Name the blood parasite species.
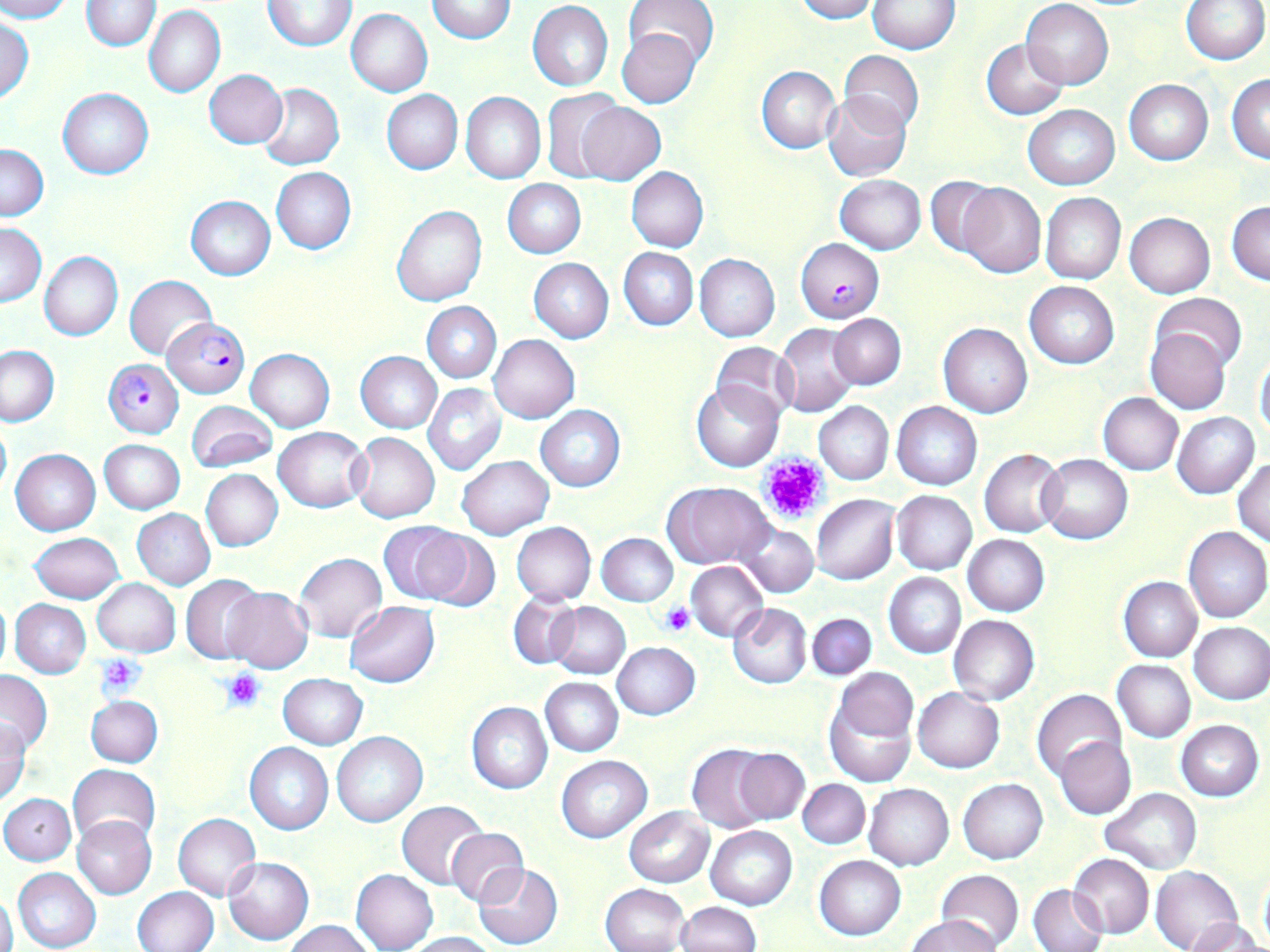

Plasmodium falciparum.

Summary:
  - Coordinate format: approximate bounding boxes as named x1/y1/x2/y2 corners in pixels
  - Uninfected red blood cell locations: (x1=0, y1=0, x2=73, y2=22), (x1=81, y1=0, x2=161, y2=50), (x1=790, y1=0, x2=877, y2=22), (x1=1021, y1=0, x2=1113, y2=89), (x1=1180, y1=0, x2=1269, y2=64), (x1=263, y1=1, x2=356, y2=51), (x1=427, y1=1, x2=516, y2=43), (x1=625, y1=1, x2=718, y2=67), (x1=867, y1=1, x2=960, y2=52), (x1=527, y1=2, x2=613, y2=90), (x1=145, y1=6, x2=226, y2=98), (x1=346, y1=9, x2=432, y2=96), (x1=0, y1=18, x2=33, y2=103), (x1=616, y1=28, x2=703, y2=109), (x1=981, y1=39, x2=1069, y2=120), (x1=837, y1=51, x2=924, y2=136), (x1=756, y1=65, x2=840, y2=152), (x1=203, y1=69, x2=287, y2=148), (x1=1228, y1=74, x2=1269, y2=163), (x1=1123, y1=79, x2=1214, y2=164), (x1=257, y1=83, x2=345, y2=170), (x1=57, y1=87, x2=153, y2=178), (x1=542, y1=87, x2=624, y2=182), (x1=381, y1=89, x2=463, y2=174), (x1=462, y1=91, x2=545, y2=184), (x1=822, y1=93, x2=912, y2=182), (x1=575, y1=100, x2=667, y2=186), (x1=1023, y1=105, x2=1120, y2=190), (x1=0, y1=143, x2=49, y2=222), (x1=271, y1=167, x2=356, y2=254), (x1=627, y1=167, x2=708, y2=252), (x1=834, y1=174, x2=927, y2=254), (x1=926, y1=175, x2=1001, y2=255), (x1=503, y1=179, x2=585, y2=257), (x1=958, y1=182, x2=1045, y2=277), (x1=1040, y1=193, x2=1126, y2=284), (x1=186, y1=196, x2=275, y2=280), (x1=1227, y1=202, x2=1270, y2=285), (x1=392, y1=206, x2=487, y2=307), (x1=1125, y1=213, x2=1215, y2=298), (x1=1, y1=221, x2=46, y2=306), (x1=618, y1=248, x2=698, y2=330), (x1=39, y1=252, x2=123, y2=342), (x1=694, y1=253, x2=779, y2=341), (x1=528, y1=258, x2=613, y2=343), (x1=125, y1=275, x2=216, y2=359), (x1=1024, y1=280, x2=1120, y2=369), (x1=1153, y1=294, x2=1248, y2=374), (x1=422, y1=302, x2=501, y2=383), (x1=829, y1=313, x2=906, y2=389), (x1=773, y1=323, x2=861, y2=416), (x1=939, y1=323, x2=1031, y2=417), (x1=1146, y1=327, x2=1230, y2=414), (x1=489, y1=334, x2=580, y2=423), (x1=711, y1=342, x2=798, y2=426), (x1=0, y1=344, x2=58, y2=426), (x1=246, y1=349, x2=333, y2=432), (x1=356, y1=351, x2=442, y2=433), (x1=1255, y1=353, x2=1270, y2=439), (x1=691, y1=381, x2=783, y2=472), (x1=422, y1=384, x2=506, y2=476), (x1=1098, y1=393, x2=1183, y2=475), (x1=186, y1=401, x2=276, y2=472), (x1=815, y1=402, x2=893, y2=484), (x1=892, y1=402, x2=982, y2=490), (x1=536, y1=406, x2=625, y2=491), (x1=1172, y1=412, x2=1259, y2=498), (x1=0, y1=417, x2=11, y2=502), (x1=273, y1=427, x2=369, y2=512), (x1=350, y1=432, x2=440, y2=522), (x1=99, y1=438, x2=185, y2=513), (x1=980, y1=448, x2=1064, y2=536), (x1=10, y1=449, x2=101, y2=536), (x1=1039, y1=454, x2=1133, y2=543), (x1=456, y1=455, x2=554, y2=539), (x1=1234, y1=458, x2=1269, y2=545), (x1=201, y1=469, x2=283, y2=552), (x1=665, y1=482, x2=774, y2=568), (x1=892, y1=491, x2=976, y2=574), (x1=812, y1=495, x2=898, y2=584), (x1=131, y1=509, x2=215, y2=590), (x1=379, y1=521, x2=475, y2=604), (x1=512, y1=522, x2=595, y2=606), (x1=737, y1=524, x2=818, y2=597), (x1=1184, y1=527, x2=1270, y2=623), (x1=412, y1=529, x2=500, y2=611), (x1=28, y1=532, x2=123, y2=603), (x1=596, y1=532, x2=678, y2=605), (x1=961, y1=534, x2=1048, y2=616), (x1=294, y1=553, x2=387, y2=643), (x1=686, y1=561, x2=769, y2=641), (x1=884, y1=572, x2=965, y2=658), (x1=182, y1=575, x2=264, y2=663), (x1=1119, y1=577, x2=1202, y2=661), (x1=92, y1=578, x2=180, y2=656), (x1=220, y1=587, x2=313, y2=673), (x1=509, y1=593, x2=580, y2=670), (x1=0, y1=595, x2=11, y2=678), (x1=11, y1=599, x2=91, y2=677), (x1=346, y1=602, x2=439, y2=688), (x1=548, y1=602, x2=630, y2=679), (x1=728, y1=604, x2=813, y2=689), (x1=807, y1=612, x2=876, y2=681), (x1=948, y1=615, x2=1039, y2=704), (x1=1189, y1=621, x2=1270, y2=704), (x1=612, y1=641, x2=699, y2=720), (x1=1112, y1=660, x2=1195, y2=743), (x1=834, y1=664, x2=919, y2=746), (x1=0, y1=670, x2=53, y2=754), (x1=278, y1=673, x2=367, y2=748), (x1=541, y1=677, x2=623, y2=756), (x1=823, y1=687, x2=916, y2=787), (x1=912, y1=688, x2=1004, y2=773), (x1=1032, y1=689, x2=1128, y2=782), (x1=85, y1=696, x2=162, y2=767), (x1=467, y1=703, x2=552, y2=794), (x1=0, y1=720, x2=31, y2=805), (x1=1175, y1=721, x2=1264, y2=800), (x1=331, y1=732, x2=427, y2=826), (x1=1055, y1=736, x2=1136, y2=819), (x1=245, y1=742, x2=333, y2=834), (x1=686, y1=745, x2=772, y2=833), (x1=733, y1=747, x2=809, y2=824), (x1=557, y1=755, x2=652, y2=842), (x1=68, y1=764, x2=160, y2=846), (x1=958, y1=778, x2=1048, y2=865), (x1=798, y1=779, x2=870, y2=849), (x1=864, y1=784, x2=954, y2=869), (x1=1101, y1=788, x2=1201, y2=874), (x1=1, y1=793, x2=75, y2=865), (x1=397, y1=801, x2=489, y2=890), (x1=624, y1=807, x2=714, y2=886), (x1=173, y1=814, x2=261, y2=900), (x1=73, y1=815, x2=156, y2=898), (x1=705, y1=826, x2=797, y2=910), (x1=447, y1=828, x2=528, y2=907), (x1=1069, y1=853, x2=1154, y2=938), (x1=815, y1=855, x2=905, y2=941), (x1=223, y1=856, x2=314, y2=945), (x1=473, y1=863, x2=564, y2=949), (x1=1152, y1=866, x2=1242, y2=952), (x1=13, y1=867, x2=102, y2=952), (x1=351, y1=868, x2=439, y2=952), (x1=936, y1=869, x2=1024, y2=950), (x1=1258, y1=871, x2=1270, y2=947), (x1=1028, y1=883, x2=1108, y2=952), (x1=601, y1=884, x2=689, y2=952), (x1=134, y1=886, x2=218, y2=952), (x1=1, y1=891, x2=18, y2=952), (x1=675, y1=901, x2=761, y2=952), (x1=904, y1=913, x2=1001, y2=952), (x1=1189, y1=916, x2=1266, y2=952), (x1=283, y1=919, x2=374, y2=951), (x1=402, y1=932, x2=501, y2=952)
  - Plasmodium falciparum-infected red blood cell locations: (x1=795, y1=238, x2=884, y2=322), (x1=162, y1=318, x2=249, y2=397), (x1=104, y1=358, x2=183, y2=438)
  - Platelet locations: (x1=757, y1=451, x2=830, y2=527), (x1=662, y1=603, x2=695, y2=636), (x1=97, y1=653, x2=147, y2=697), (x1=220, y1=669, x2=265, y2=713)
  - Modality: light microscopy
  - Stain: May-Grünwald-Giemsa
  - Preparation: thin blood film
  - Field of view: single
  - Magnification: 1000x
  - Image size: 1270×952 pixels